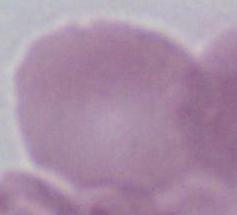
Summary:
  - Magnification: 1000x
  - Modality: photomicrograph
  - Identification: erythrocyte